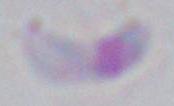
Summary:
  - Modality: micrograph
  - Identification: Toxoplasma gondii
  - Magnification: 1000x